Mark where leukocytes are.
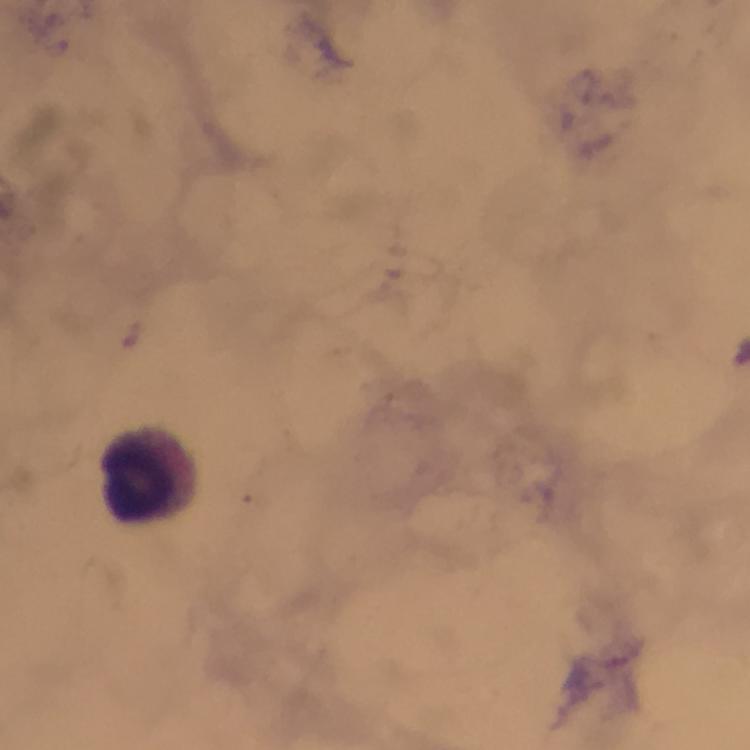

Approximate centers as [x, y] in pixels.
Leukocytes: [145, 480].

{
  "magnification": "100x",
  "stain": "Giemsa",
  "preparation": "thick blood film",
  "malaria_parasites": "none seen",
  "context": "from a malaria diagnostic workup",
  "cropped_from": "a single field of view",
  "image_size": "750×750 pixels",
  "capture": "smartphone mounted on the microscope",
  "immersion_oil": "used"
}